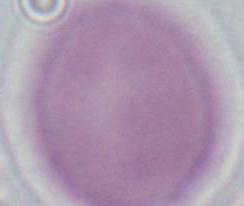
Summary:
  - Magnification: 1000x
  - Modality: micrograph
  - Identification: red blood cell